Report the malaria status of this cell.
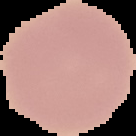
Uninfected.

From a thin blood smear. Cell region segmented out of the field of view; the surrounding area is masked to black. Image is 136×136 pixels.